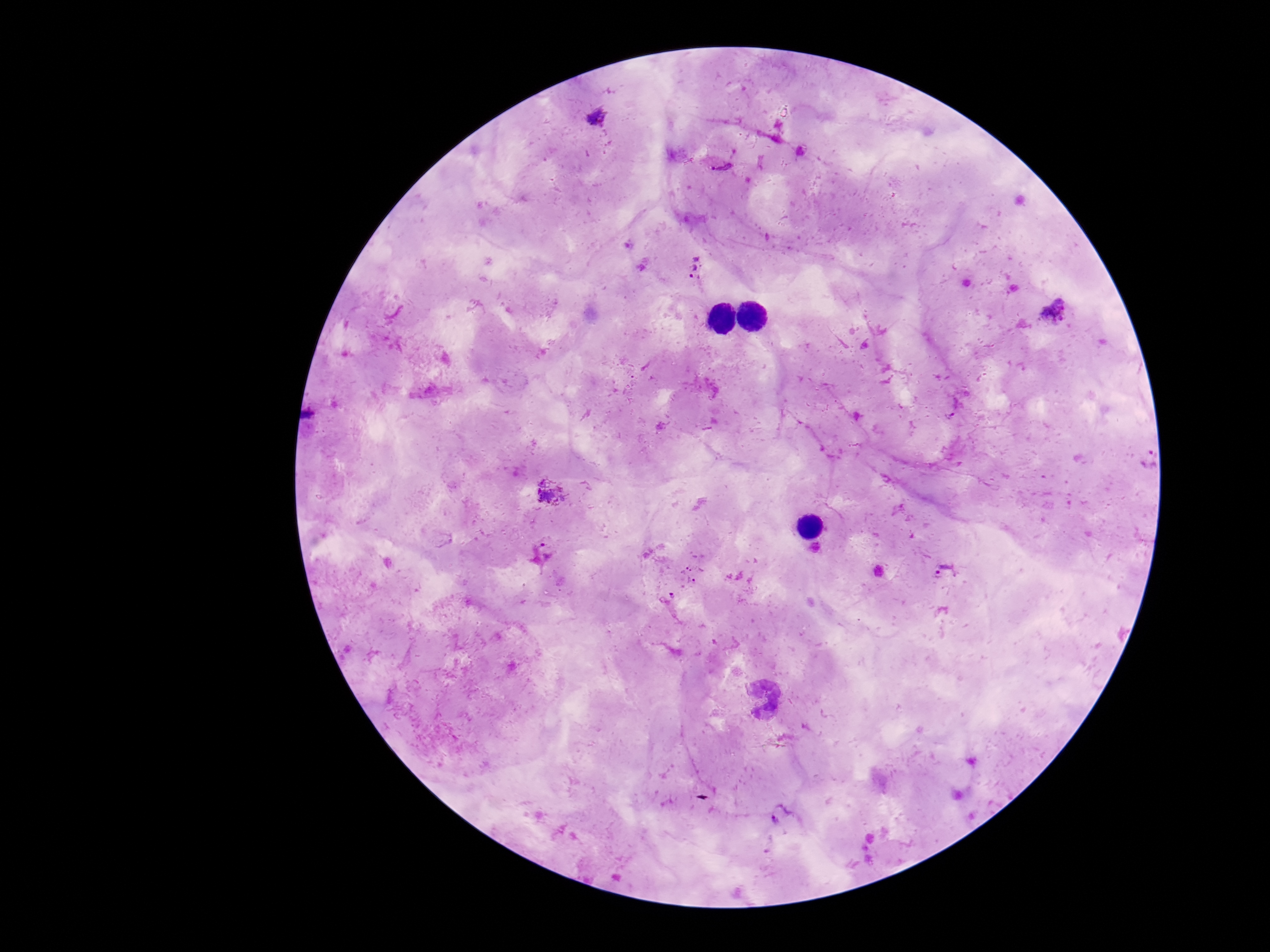

Approximate centers as [x, y] in pixels.
Summary:
  - Plasmodium parasite locations: [596, 118], [721, 161], [696, 268], [1053, 310], [1147, 458], [550, 491], [548, 550], [945, 570], [693, 574], [667, 597], [781, 813]
  - Capture: smartphone camera through the microscope eyepiece
  - Field of view: single
  - Image size: 1270×952 pixels
  - Stain: Giemsa
  - Magnification: 100x
  - Patient malaria status: infected
  - Preparation: thick blood film